Assess the morphology of the erythrocytes.
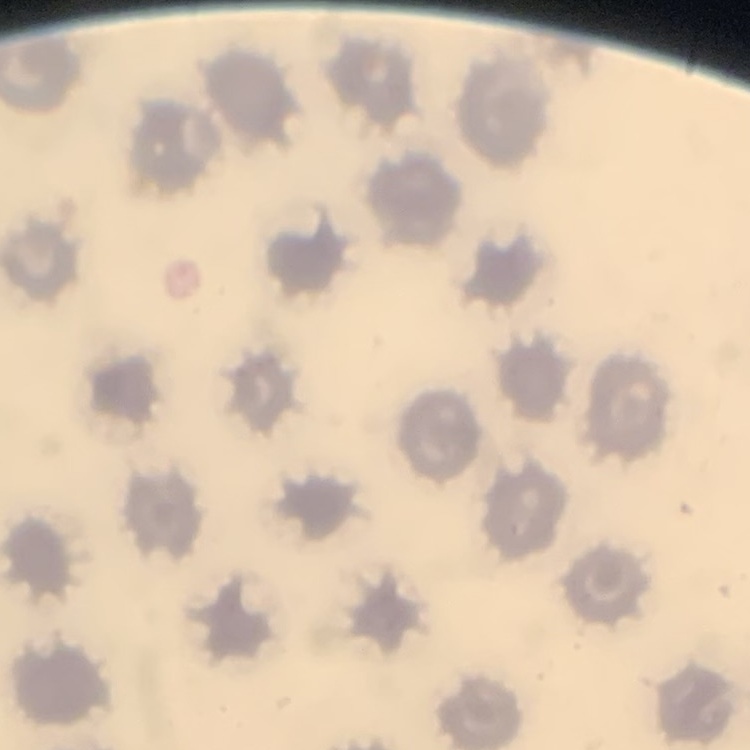

No rouleaux formation.

Square crop of a larger photomicrograph. Thin blood smear. Field's or Giemsa stain.